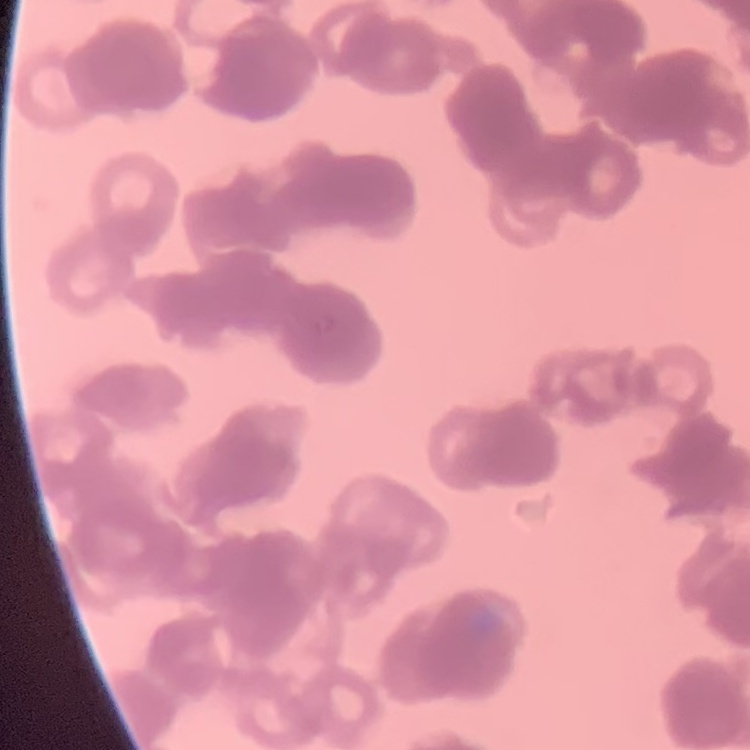 The red blood cells exhibit rouleaux formation. Square crop of a larger photomicrograph. Thin blood smear. Field's or Giemsa stain.